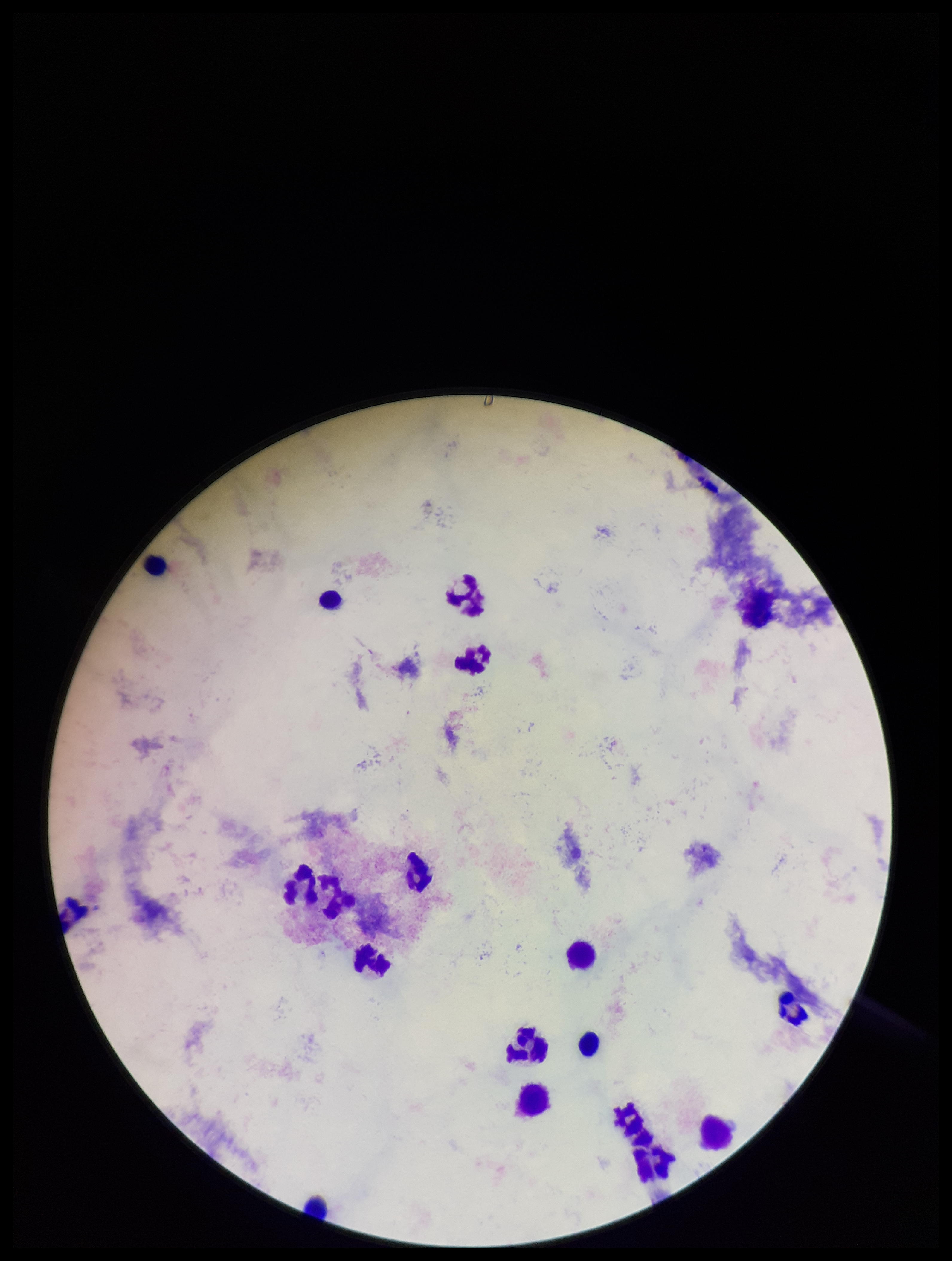 Leukocyte count: 18. Stained with Giemsa. Parasite count: 0. Single field of view. Patient malaria status: negative. Plasmodium parasites: none detected. Image is 952×1261 pixels. Smartphone photograph taken through the eyepiece of a microscope. Preparation: thick smear.